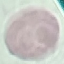

Malaria status: uninfected. Giemsa stain. Cell patch, automatically extracted from a larger field of view and resized to 64 × 64 pixels. Thin smear of blood. Photographed with a smartphone camera at the microscope eyepiece.